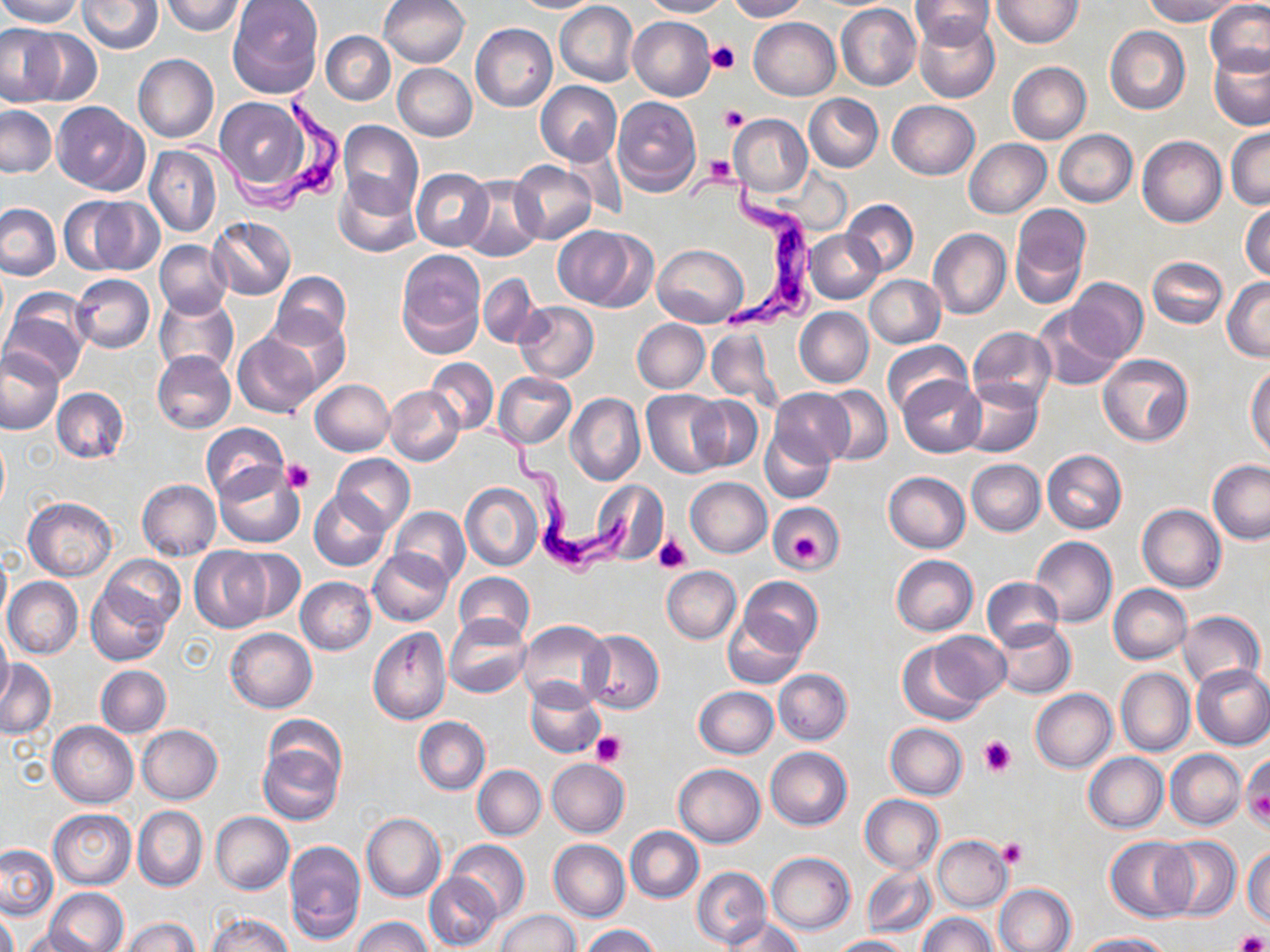
Approximate bounding boxes as (x1,y1)-(x2,y2) corner pairs in pixels. Trypanosoma brucei locations: (179,86)-(350,219), (683,165)-(823,336), (469,412)-(636,586). Uninfected red blood cell locations: (0,0)-(83,27), (78,0)-(162,52), (159,0)-(247,35), (379,0)-(469,69), (513,0)-(600,13), (641,0)-(730,18), (726,0)-(807,22), (909,0)-(997,48), (1143,0)-(1242,25), (227,1)-(322,97), (991,1)-(1082,48), (1205,1)-(1270,78), (555,2)-(639,86), (835,3)-(921,90), (628,16)-(716,100), (913,17)-(999,103), (749,18)-(840,101), (470,23)-(557,113), (1104,25)-(1190,114), (0,26)-(65,106), (22,27)-(101,106), (321,31)-(395,105), (1208,45)-(1270,129), (134,53)-(218,143), (1007,61)-(1091,144), (391,63)-(477,141), (535,81)-(623,166), (804,93)-(883,172), (214,95)-(314,194), (612,97)-(701,197), (887,100)-(980,179), (52,102)-(148,195), (1,105)-(56,177), (729,114)-(812,195), (338,120)-(423,218), (1226,126)-(1269,210), (1054,130)-(1137,207), (1138,136)-(1226,227), (964,138)-(1051,218), (559,143)-(628,220), (145,145)-(221,237), (509,161)-(597,244), (412,169)-(494,251), (459,176)-(545,261), (336,177)-(418,257), (82,197)-(164,275), (842,200)-(919,276), (1241,201)-(1269,282), (0,203)-(61,279), (1009,205)-(1090,308), (207,216)-(295,300), (552,225)-(653,310), (928,228)-(1011,319), (806,230)-(884,304), (155,240)-(233,318), (653,244)-(749,325), (396,251)-(486,357), (1147,257)-(1227,328), (270,271)-(351,347), (479,272)-(539,348), (71,273)-(155,354), (865,275)-(944,349), (1065,277)-(1147,363), (1222,277)-(1270,361), (2,289)-(92,385), (154,295)-(239,378), (513,301)-(598,383), (1034,305)-(1121,390), (794,307)-(874,387), (267,312)-(347,393), (632,318)-(710,393), (706,327)-(777,406), (968,327)-(1056,408), (232,332)-(323,419), (882,341)-(970,418), (0,346)-(66,436), (153,350)-(237,434), (1098,355)-(1193,447), (426,358)-(499,434), (1247,365)-(1270,455), (494,372)-(575,449), (898,376)-(984,457), (311,378)-(395,455), (958,379)-(1042,457), (384,385)-(464,466), (819,386)-(892,465), (52,387)-(128,464), (642,389)-(730,478), (769,389)-(854,466), (567,394)-(645,485), (688,396)-(763,472), (200,422)-(289,504), (761,427)-(837,503), (0,431)-(9,516), (1042,449)-(1127,534), (331,454)-(415,535), (966,459)-(1046,536), (1207,460)-(1269,545), (213,463)-(304,548), (883,471)-(970,553), (684,477)-(771,558), (591,478)-(669,564), (138,479)-(221,561), (461,483)-(543,571), (309,490)-(392,571), (22,498)-(116,581), (770,504)-(843,573), (1137,504)-(1226,592), (391,506)-(470,585), (1030,536)-(1117,627), (189,547)-(271,633), (230,548)-(305,624), (368,548)-(453,626), (0,549)-(10,628), (100,554)-(184,629), (890,555)-(978,636), (662,566)-(740,644), (456,571)-(535,642), (3,577)-(83,659), (296,577)-(377,655), (738,577)-(822,655), (982,578)-(1063,651), (1108,584)-(1192,664), (86,585)-(172,666), (1178,610)-(1265,690), (724,612)-(807,687), (445,614)-(531,696), (517,620)-(613,709), (992,621)-(1074,698), (226,627)-(317,712), (367,627)-(450,725), (0,629)-(13,705), (581,629)-(664,713), (931,630)-(1011,706), (898,639)-(991,725), (0,659)-(56,739), (1192,664)-(1270,749), (96,665)-(171,737), (1115,667)-(1195,756), (774,669)-(852,744), (525,681)-(604,757), (693,686)-(779,758), (1031,689)-(1117,772), (263,713)-(346,791), (414,717)-(490,795), (48,721)-(138,808), (886,722)-(967,798), (137,724)-(223,804), (256,739)-(344,825), (765,747)-(852,831), (1166,749)-(1246,830), (1084,753)-(1168,832), (1242,754)-(1270,833), (546,758)-(629,838), (673,763)-(765,847), (473,766)-(546,839), (859,795)-(944,874), (133,806)-(206,891), (48,809)-(136,889), (210,812)-(293,895), (361,812)-(446,901), (625,827)-(704,903), (932,835)-(1012,912), (1158,836)-(1241,919), (1105,837)-(1194,921), (549,839)-(630,921), (284,840)-(366,944), (446,840)-(529,922), (1,846)-(58,920), (1244,846)-(1270,928), (765,851)-(856,935), (861,865)-(938,938), (692,867)-(771,949), (424,872)-(501,951), (994,883)-(1075,952), (44,889)-(129,951), (0,908)-(18,952), (496,909)-(578,952), (209,912)-(292,952), (919,912)-(996,952), (721,915)-(804,952), (353,916)-(432,952), (121,917)-(199,952), (582,926)-(660,952), (19,928)-(96,951), (1075,933)-(1170,952), (830,935)-(909,951). Platelet locations: (708,42)-(740,73), (719,105)-(749,132), (706,155)-(737,186), (283,458)-(313,493), (655,534)-(690,573), (791,535)-(823,565), (591,731)-(626,767), (977,736)-(1016,777), (1242,764)-(1270,829), (999,838)-(1026,868), (1234,931)-(1269,952). Slide-level diagnosis: Trypanosoma brucei. Light microscopy. One field of a larger specimen. Thin blood smear. 1000x magnification. Image is 1270×952 pixels. May-Grünwald-Giemsa-stained preparation.